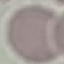
{
  "result": "negative for malaria parasites",
  "stain": "Giemsa",
  "capture": "smartphone through the microscope eyepiece",
  "preparation": "thin blood film",
  "image_type": "cell patch, automatically extracted from a larger field of view and resized to 64 × 64 pixels"
}